Describe the morphology of the erythrocytes.
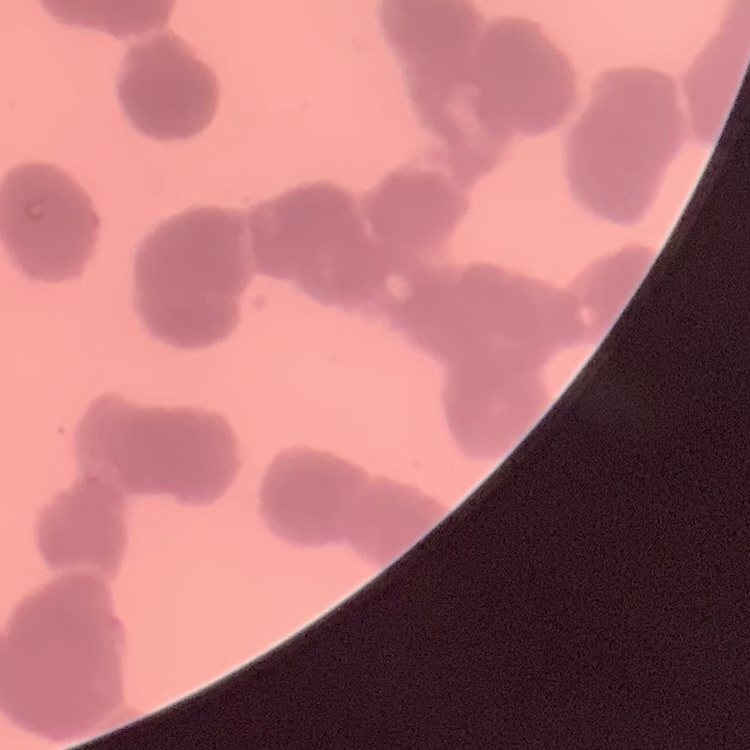
They show rouleaux formation.

Summary:
  - Stain: Field's or Giemsa
  - Preparation: thin blood film
  - Image type: one tile cut from a larger photomicrograph